Identify the preparation type.
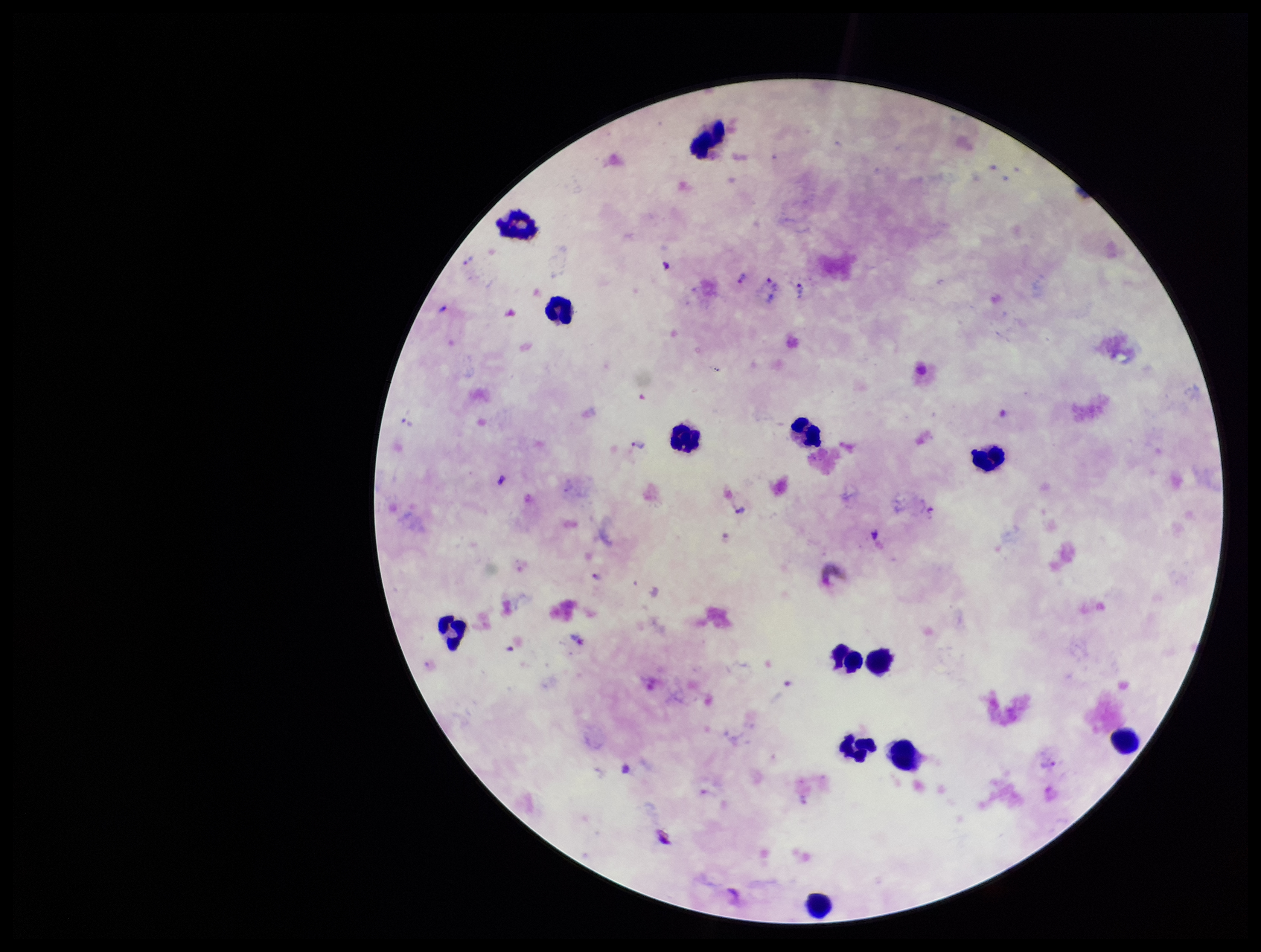
Thick.

image size = 1261×952 pixels
field of view = single
parasite count = 4
species reported for this patient = Plasmodium vivax
capture = smartphone photograph through the microscope eyepiece
patient malaria status = positive
stain = Giemsa
leukocyte count = 13
Plasmodium parasites = detected